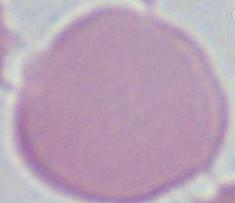 1000x magnification. A red blood cell is seen. Micrograph.